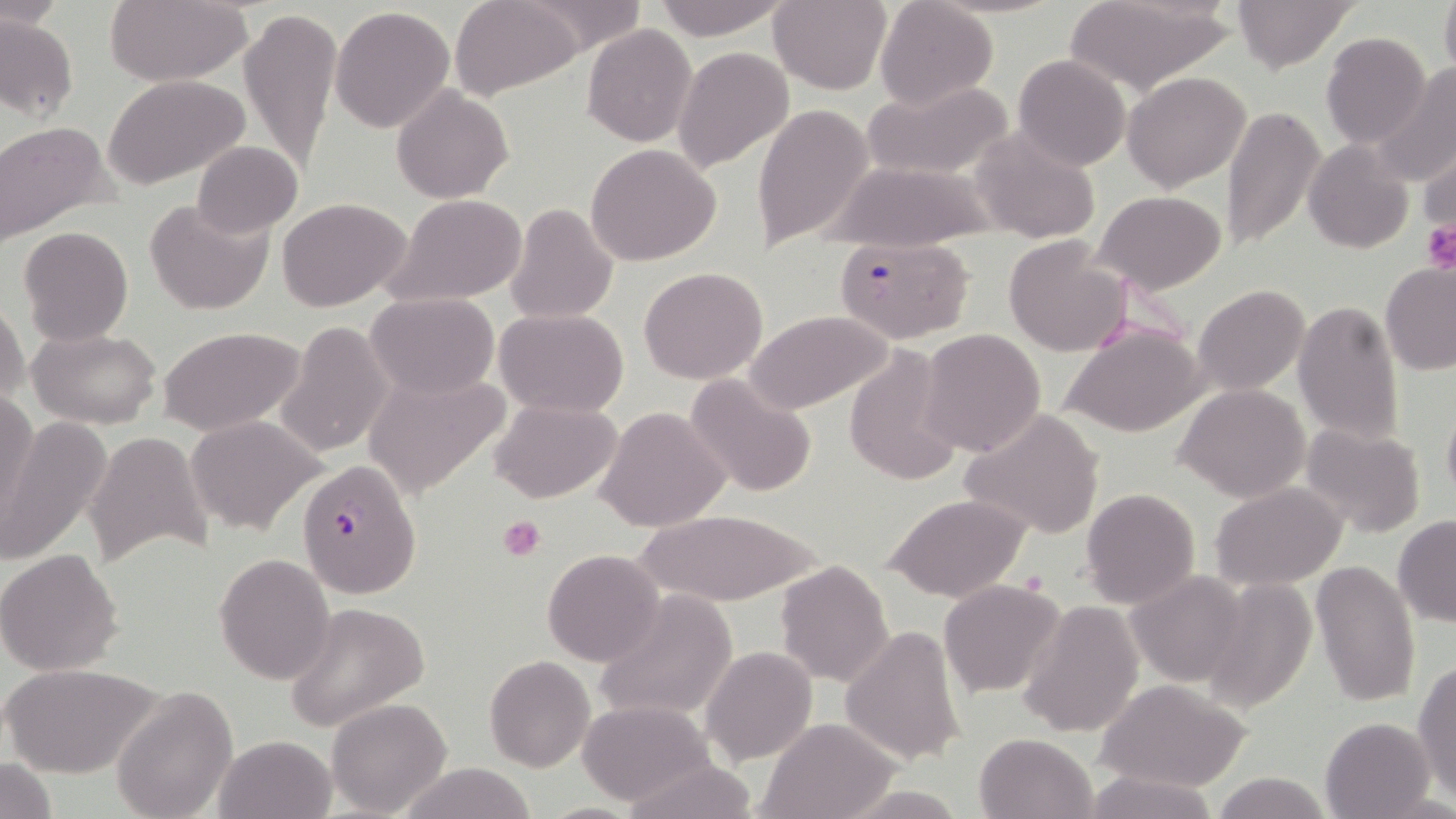
Summary:
  - Coordinate format: approximate bounding boxes as (x1, y1, x2, y2) in pixels
  - Plasmodium falciparum-infected red blood cell locations: (833, 236, 975, 345), (295, 459, 422, 599)
  - Platelet locations: (1421, 219, 1456, 274), (498, 514, 546, 561)
  - Uninfected red blood cell locations: (103, 0, 251, 86), (452, 0, 584, 99), (650, 0, 790, 41), (768, 0, 892, 95), (1062, 0, 1235, 99), (1232, 0, 1356, 71), (1439, 0, 1456, 80), (520, 1, 650, 55), (874, 1, 999, 109), (240, 5, 341, 173), (332, 7, 456, 131), (0, 12, 78, 121), (583, 24, 698, 147), (1321, 33, 1431, 149), (673, 46, 794, 172), (1013, 55, 1130, 171), (1373, 64, 1456, 191), (1122, 71, 1251, 192), (102, 73, 252, 191), (863, 80, 1014, 181), (392, 87, 512, 203), (752, 102, 873, 253), (1220, 104, 1325, 253), (0, 120, 116, 248), (971, 124, 1101, 245), (191, 141, 303, 237), (1303, 141, 1414, 254), (1417, 141, 1456, 238), (586, 144, 722, 266), (828, 161, 1001, 251), (1093, 190, 1227, 293), (145, 195, 274, 316), (385, 195, 528, 307), (278, 198, 410, 313), (505, 203, 618, 324), (19, 225, 133, 345), (1003, 237, 1132, 357), (1379, 261, 1456, 375), (638, 267, 767, 384), (1194, 285, 1310, 396), (365, 292, 500, 401), (0, 298, 28, 410), (1294, 301, 1407, 445), (495, 310, 627, 418), (744, 311, 891, 413), (274, 321, 393, 458), (1061, 323, 1209, 439), (29, 326, 160, 427), (159, 326, 307, 437), (918, 329, 1047, 457), (843, 346, 966, 487), (363, 366, 513, 500), (687, 373, 817, 498), (1176, 383, 1312, 501), (2, 390, 40, 523), (1441, 395, 1456, 511), (490, 398, 621, 503), (596, 406, 731, 533), (961, 408, 1106, 540), (2, 414, 111, 568), (185, 416, 325, 536), (1301, 422, 1428, 537), (85, 429, 213, 565), (1212, 482, 1348, 588), (1080, 488, 1199, 608), (885, 494, 1032, 604), (634, 509, 820, 605), (1393, 513, 1456, 629), (0, 548, 125, 676), (541, 548, 666, 668), (214, 552, 336, 685), (774, 559, 894, 687), (1311, 561, 1421, 709), (1126, 571, 1249, 687), (1204, 575, 1316, 715), (940, 579, 1067, 698), (593, 588, 739, 724), (282, 601, 429, 733), (1017, 604, 1143, 739), (840, 626, 966, 765), (701, 647, 816, 765), (485, 655, 594, 771), (1414, 659, 1456, 800), (2, 661, 159, 778), (1095, 677, 1254, 792), (109, 686, 238, 819), (326, 697, 453, 818), (576, 699, 715, 807), (1320, 716, 1436, 819), (758, 717, 902, 819), (975, 732, 1096, 818), (215, 735, 338, 819), (1, 756, 57, 819), (617, 759, 763, 819), (395, 762, 539, 819), (1083, 769, 1220, 819), (1213, 770, 1330, 819), (532, 802, 653, 819)
  - Slide-level diagnosis: Plasmodium falciparum
  - Magnification: 1000x
  - Preparation: thin blood smear
  - Field of view: single
  - Image size: 1456×819 pixels
  - Stain: May-Grünwald-Giemsa
  - Modality: light microscopy